Locate every leukocyte (white blood cell).
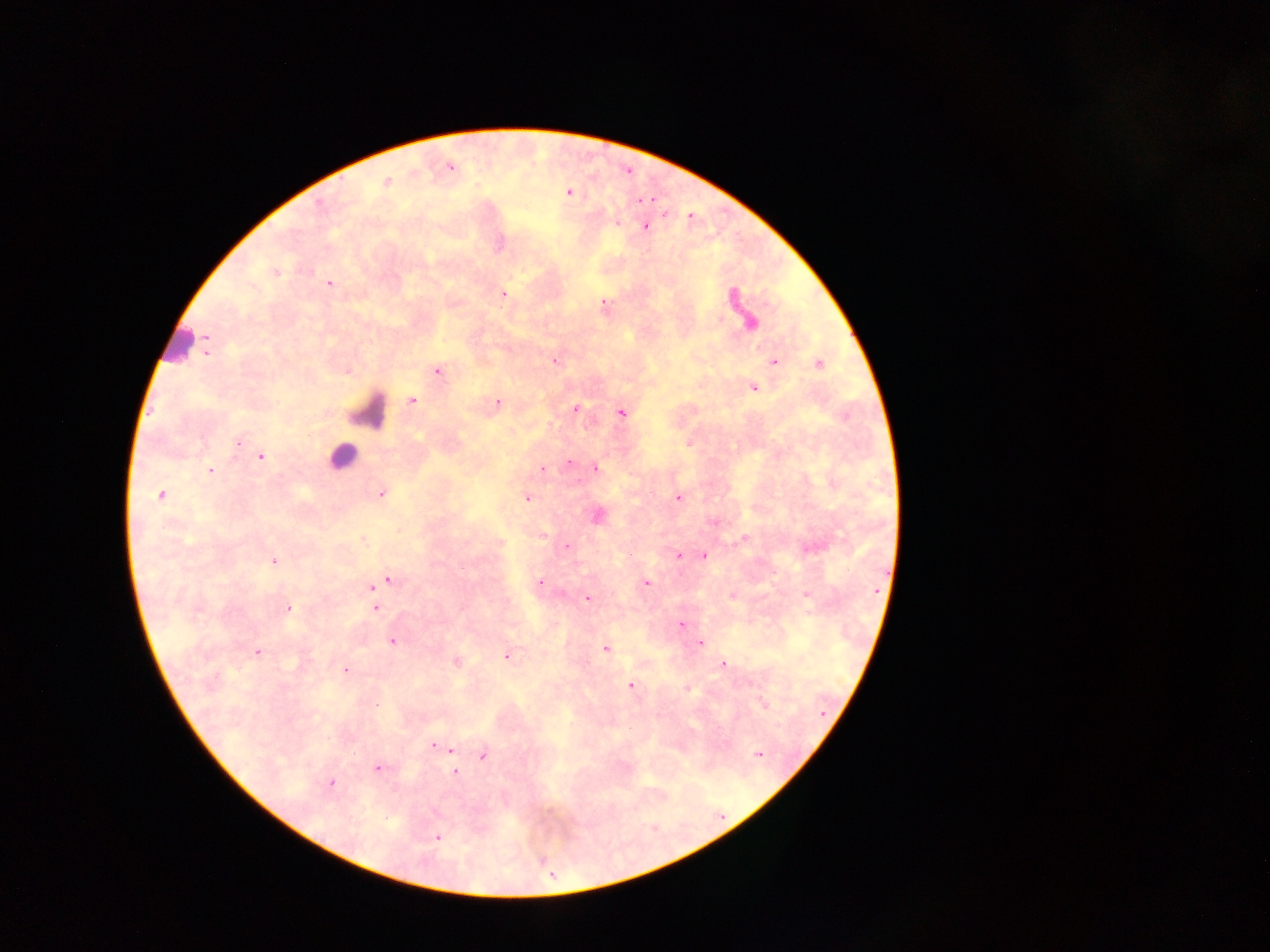

Approximate centers as (x, y) in pixels.
Leukocytes: (176, 350), (370, 405), (342, 459).

Malaria parasite locations: (387, 182), (568, 193), (637, 201), (644, 227), (276, 273), (328, 283), (504, 292), (206, 353), (552, 359), (772, 361), (818, 362), (437, 371), (753, 389), (413, 400), (496, 403), (576, 407), (622, 414), (687, 443), (239, 444), (259, 457), (569, 464), (594, 468), (542, 470), (211, 471), (381, 494), (161, 496), (678, 497), (527, 498), (595, 516), (542, 534), (743, 535), (361, 539), (566, 546), (678, 555), (702, 557), (275, 561), (541, 581), (645, 582), (377, 583), (805, 595), (733, 597), (588, 598), (374, 602), (289, 608), (679, 624), (392, 642), (702, 644), (606, 647), (258, 653), (505, 656), (456, 662), (723, 662), (346, 671), (630, 685), (686, 688), (434, 743), (450, 749), (483, 756), (377, 768), (456, 773), (330, 784), (437, 837). Photographed through a microscope with a mobile-phone camera. Image is 1270×952 pixels. Thick blood smear. One field of view. Collected in Ghana.